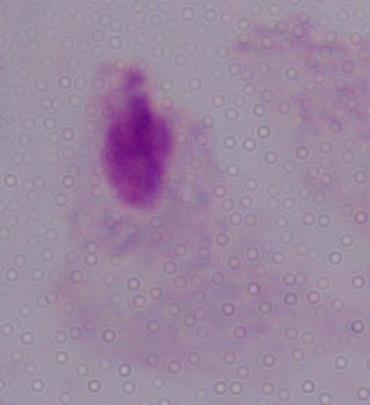

modality = micrograph
magnification = 1000x
identification = trichomonad